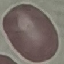

malaria status = uninfected
preparation = thin blood smear
stain = Giemsa
capture = smartphone through the microscope eyepiece
image type = automatically extracted cell patch, resized to 64 × 64 pixels